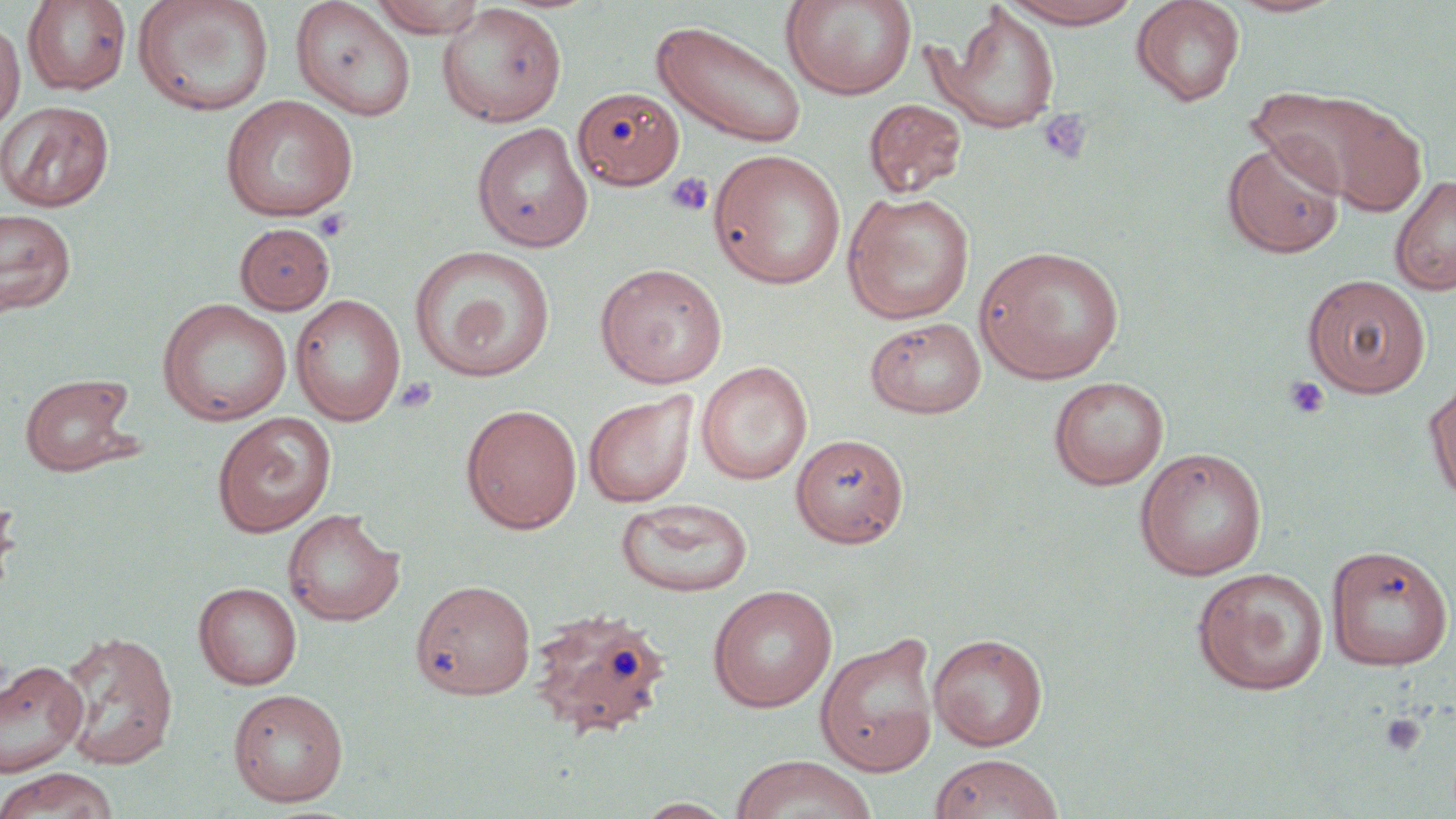

Approximate bounding boxes as named x1/y1/x2/y2 corners in pixels. Platelet locations: (x1=1037, y1=109, x2=1093, y2=165), (x1=665, y1=172, x2=712, y2=216), (x1=315, y1=208, x2=351, y2=241), (x1=1283, y1=375, x2=1329, y2=420), (x1=394, y1=376, x2=437, y2=414), (x1=1379, y1=712, x2=1426, y2=756). Uninfected red blood cell locations: (x1=22, y1=0, x2=132, y2=95), (x1=132, y1=0, x2=275, y2=117), (x1=369, y1=0, x2=487, y2=37), (x1=781, y1=0, x2=917, y2=101), (x1=1000, y1=0, x2=1146, y2=28), (x1=1130, y1=0, x2=1246, y2=106), (x1=1226, y1=0, x2=1343, y2=18), (x1=289, y1=1, x2=416, y2=121), (x1=436, y1=2, x2=567, y2=127), (x1=931, y1=3, x2=1062, y2=134), (x1=651, y1=19, x2=808, y2=147), (x1=0, y1=20, x2=25, y2=131), (x1=1248, y1=84, x2=1420, y2=209), (x1=571, y1=86, x2=685, y2=190), (x1=220, y1=94, x2=359, y2=221), (x1=864, y1=98, x2=968, y2=198), (x1=0, y1=100, x2=115, y2=212), (x1=471, y1=121, x2=593, y2=252), (x1=1222, y1=137, x2=1346, y2=258), (x1=708, y1=149, x2=847, y2=290), (x1=1389, y1=173, x2=1456, y2=297), (x1=842, y1=191, x2=975, y2=324), (x1=0, y1=208, x2=77, y2=315), (x1=234, y1=222, x2=335, y2=315), (x1=975, y1=244, x2=1125, y2=384), (x1=409, y1=245, x2=556, y2=382), (x1=593, y1=262, x2=728, y2=388), (x1=1302, y1=273, x2=1431, y2=397), (x1=290, y1=293, x2=405, y2=426), (x1=156, y1=298, x2=293, y2=426), (x1=865, y1=316, x2=986, y2=419), (x1=696, y1=361, x2=812, y2=485), (x1=20, y1=373, x2=138, y2=477), (x1=1048, y1=376, x2=1170, y2=490), (x1=1424, y1=376, x2=1456, y2=509), (x1=583, y1=391, x2=698, y2=507), (x1=460, y1=403, x2=582, y2=534), (x1=212, y1=412, x2=336, y2=537), (x1=791, y1=433, x2=909, y2=547), (x1=1134, y1=447, x2=1268, y2=581), (x1=0, y1=488, x2=21, y2=606), (x1=615, y1=497, x2=754, y2=598), (x1=282, y1=508, x2=404, y2=626), (x1=1326, y1=544, x2=1454, y2=671), (x1=1191, y1=567, x2=1329, y2=696), (x1=410, y1=579, x2=537, y2=700), (x1=193, y1=582, x2=302, y2=690), (x1=707, y1=584, x2=838, y2=712), (x1=526, y1=606, x2=672, y2=740), (x1=56, y1=630, x2=178, y2=769), (x1=815, y1=632, x2=941, y2=777), (x1=928, y1=632, x2=1049, y2=751), (x1=0, y1=659, x2=89, y2=778), (x1=227, y1=688, x2=348, y2=807), (x1=728, y1=754, x2=879, y2=819), (x1=929, y1=754, x2=1064, y2=819), (x1=0, y1=767, x2=120, y2=819), (x1=631, y1=797, x2=738, y2=818). Slide-level diagnosis: no evidence of blood parasites. Image is 1456×819 pixels. May-Grünwald-Giemsa-stained preparation. Optical microscopy. Single field of view. Thin blood smear. Captured at 1000x magnification.